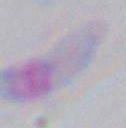

Micrograph. 1000x magnification. Toxoplasma gondii is seen.